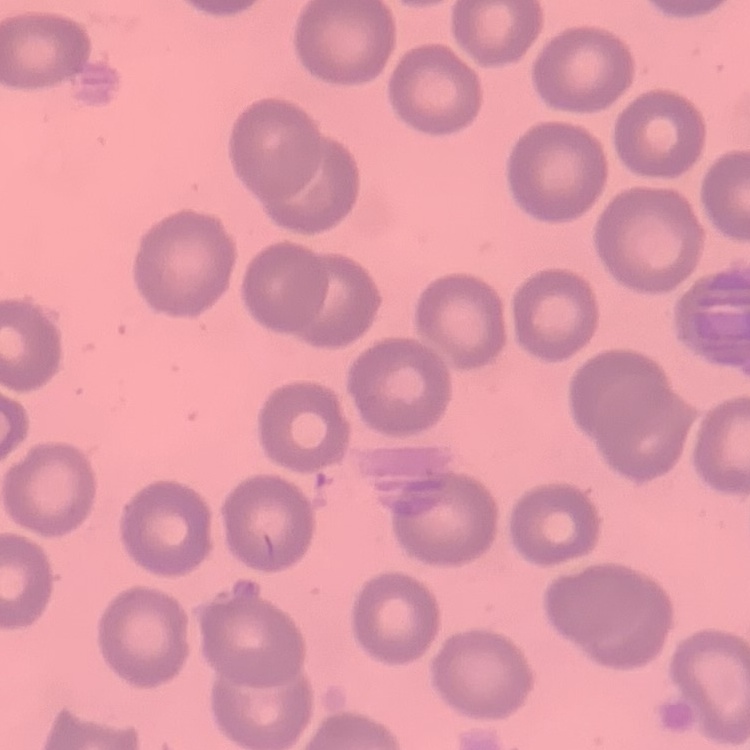
Summary:
  - Red blood cell morphology: no rouleaux formation
  - Preparation: thin peripheral smear
  - Image type: one tile cut from a larger photomicrograph
  - Stain: Field's or Giemsa